Give the position of every malaria parasite.
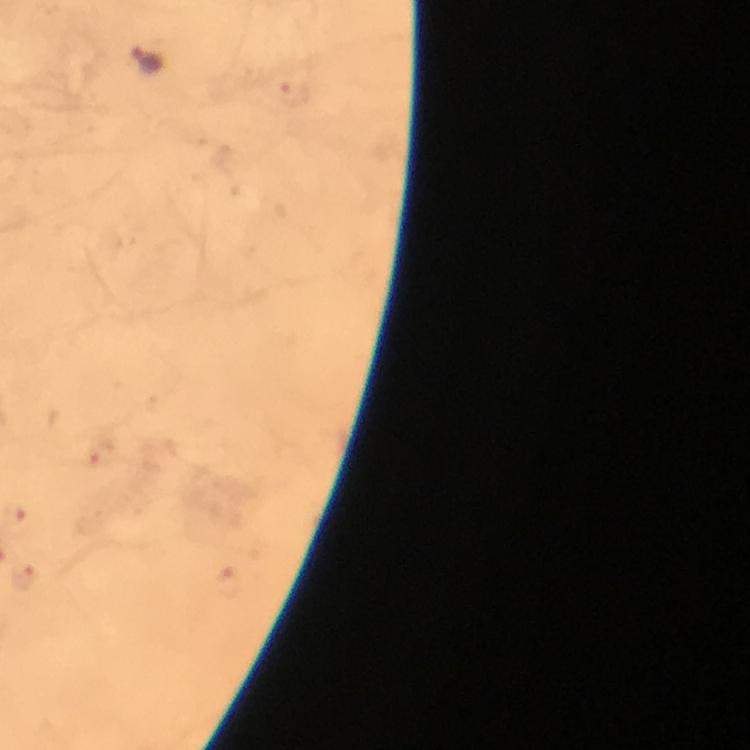

Approximate centers as (x, y) in pixels.
Malaria parasites: (147, 60), (107, 452), (27, 579), (230, 579).

magnification = 100x
capture = smartphone camera through the microscope
cropped from = one field of view
immersion oil = applied
preparation = thick blood smear
context = from a malaria diagnostic workup
stain = Giemsa
image size = 750×750 pixels